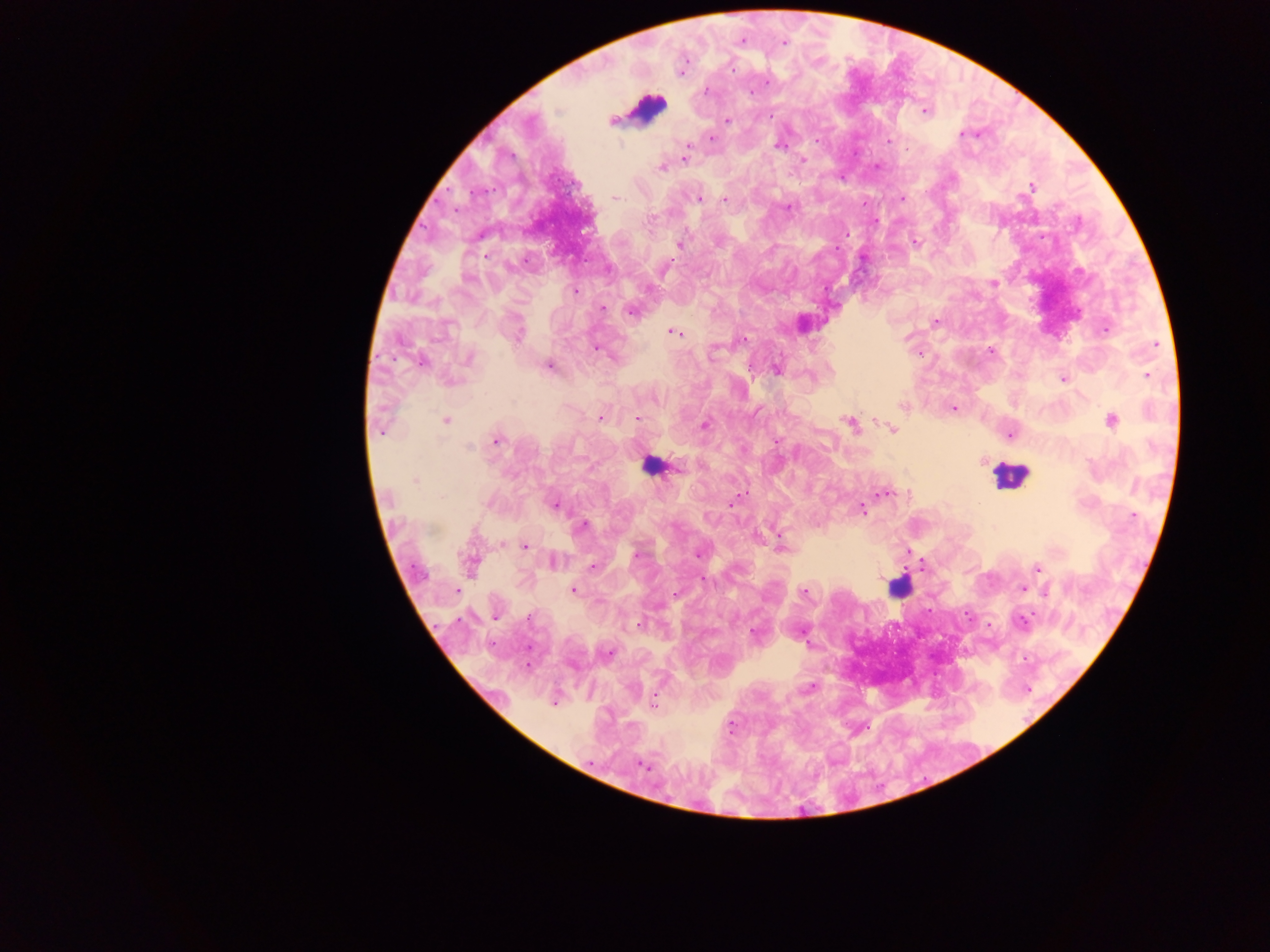
Approximate centers as x y in pixels. Leukocyte locations: 647 109; 650 467; 1008 474; 899 587. Plasmodium parasite locations: 742 40; 784 42; 732 68; 681 71; 706 91; 750 92; 558 110; 924 111; 728 119; 612 121; 963 134; 711 138; 887 140; 687 145; 779 146; 685 152; 684 158; 802 160; 661 168; 1031 186; 616 197; 700 199; 725 199; 902 199; 788 207; 847 233; 917 242; 680 244; 467 278; 993 284; 574 291; 603 308; 632 311; 935 323; 1105 330; 674 332; 517 333; 743 340; 595 349; 991 351; 468 358; 420 363; 548 366; 777 370; 1147 375; 1062 379; 902 406; 953 409; 601 417; 637 419; 1111 420; 446 421; 850 423; 704 426; 892 429; 380 432; 1011 435; 496 441; 776 442; 468 447; 415 482; 886 492; 731 502; 554 505; 862 509; 1134 516; 583 525; 524 546; 781 546; 909 552; 636 554; 697 554; 553 562; 470 564; 592 566; 1037 568; 1022 588; 457 590; 574 590; 1046 592; 676 593; 804 593; 495 617; 1022 621; 638 624; 608 653; 809 689; 554 703; 653 704; 731 726; 642 766. Photographed through a microscope with a mobile-phone camera. One field of view. Image is 1270×952 pixels. Thick blood film. Sample from Ghana.